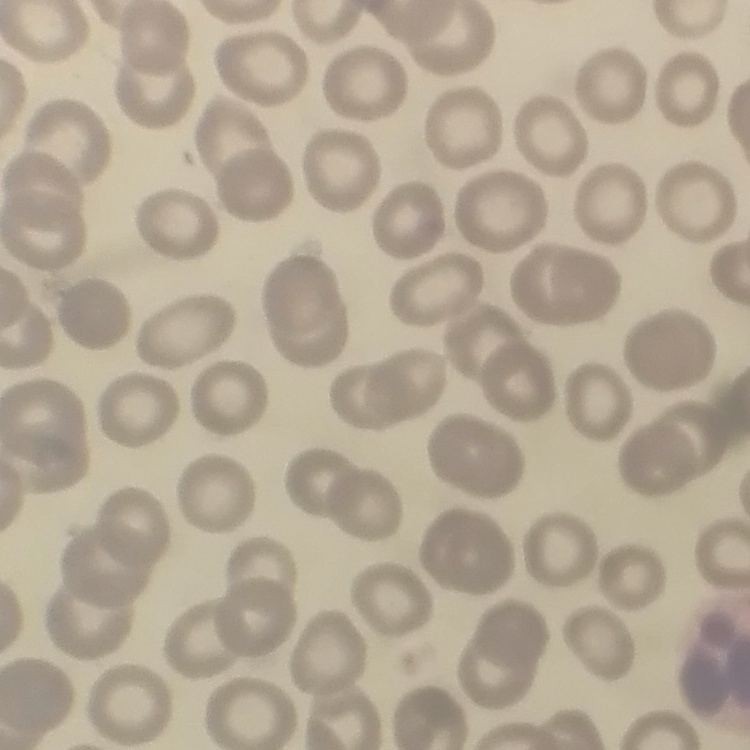
{
  "erythrocyte_morphology": "no rouleaux formation",
  "image_type": "one tile cut from a larger photomicrograph",
  "stain": "Field's or Giemsa",
  "preparation": "thin blood film"
}